Report the malaria status of this cell.
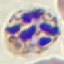
It is parasitized.

Summary:
  - Preparation: thin smear
  - Capture: smartphone through the microscope eyepiece
  - Stain: Giemsa
  - Image type: automatically extracted cell patch, resized to 64 × 64 pixels